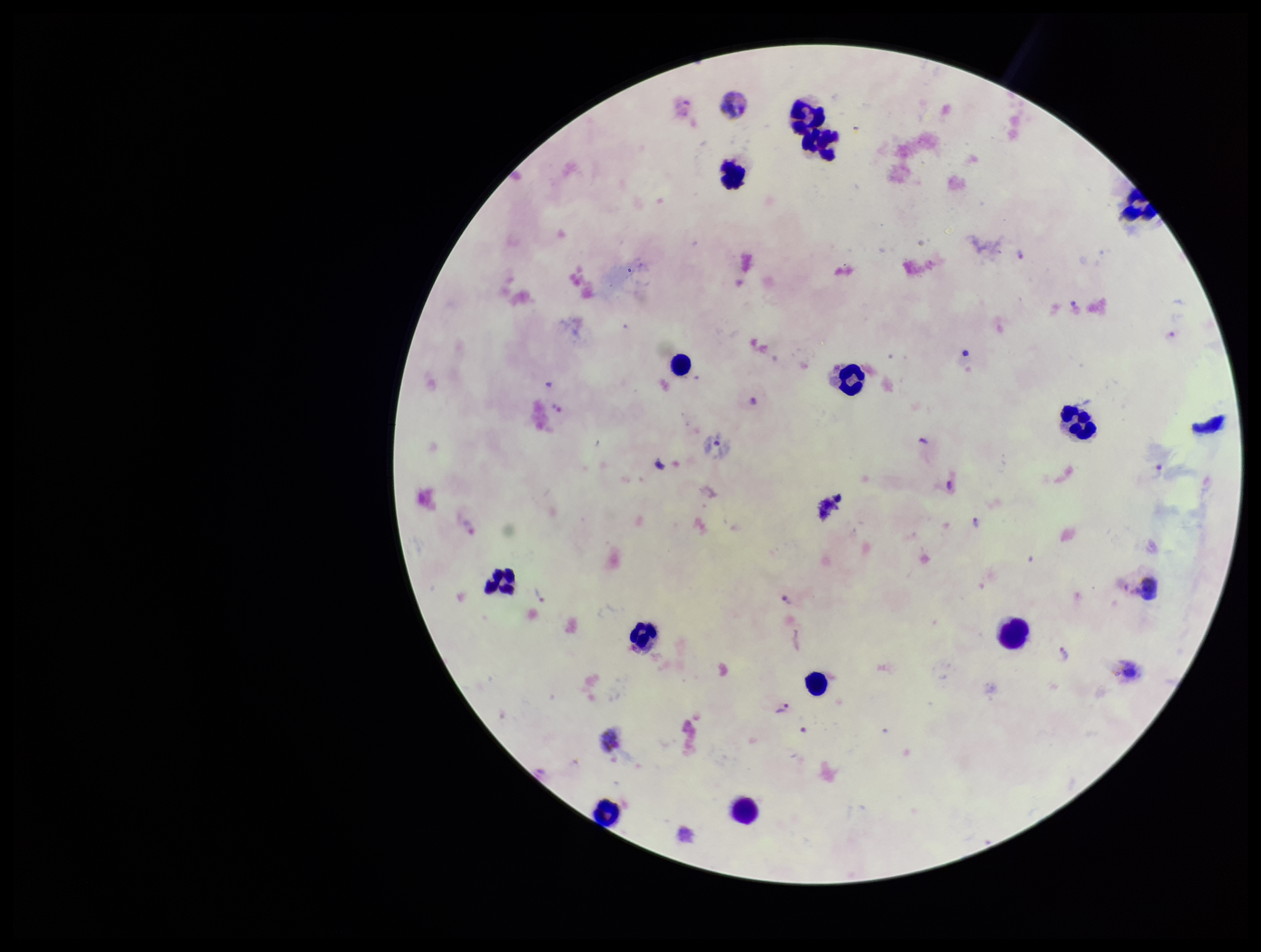

Summary:
  - Leukocyte count: 15
  - Capture: smartphone photograph through the microscope eyepiece
  - Plasmodium parasites: detected
  - Image size: 1261×952 pixels
  - Species reported for this patient: Plasmodium vivax
  - Parasite count: 11
  - Stain: Giemsa
  - Patient malaria status: infected
  - Preparation: thick smear
  - Field of view: one from this slide